Classify this cell by malaria status.
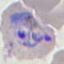

Parasitized.

{
  "capture": "smartphone camera at the microscope eyepiece",
  "stain": "Giemsa",
  "image_type": "cell patch, automatically extracted from a larger field of view and resized to 64 × 64 pixels",
  "preparation": "thin blood film"
}